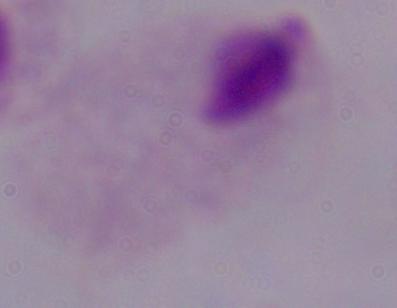
Summary:
  - Magnification: 1000x
  - Identification: trichomonad
  - Modality: micrograph